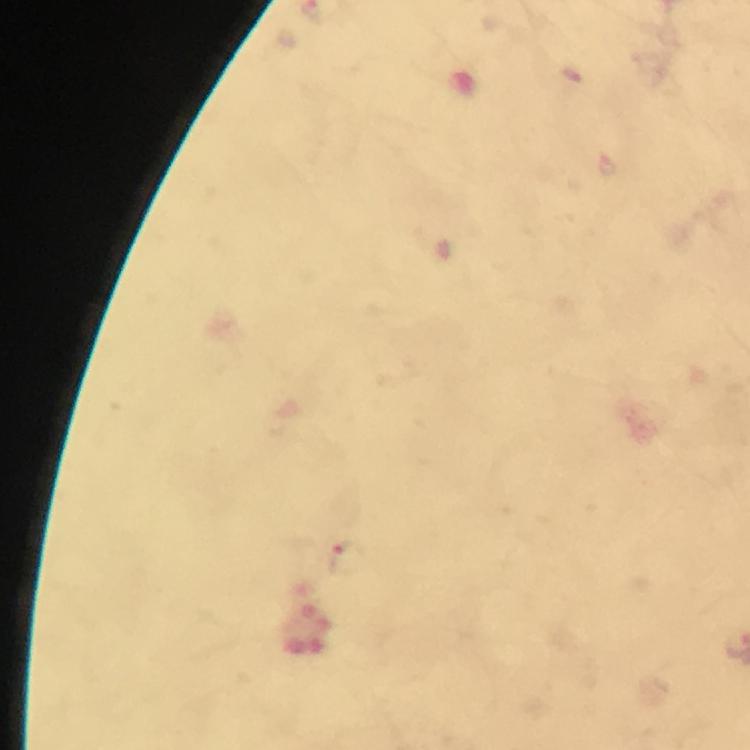
Approximate centers as [x, y] in pixels. Plasmodium parasite locations: [348, 559]. At 100x magnification. Giemsa stain. Cropped region of a single field of view. Thick blood film. From a diagnostic examination for malaria. Immersion oil was used. Photographed through the microscope with a smartphone camera. Image is 750×750 pixels.